Give the extent of all Trypanosoma brucei.
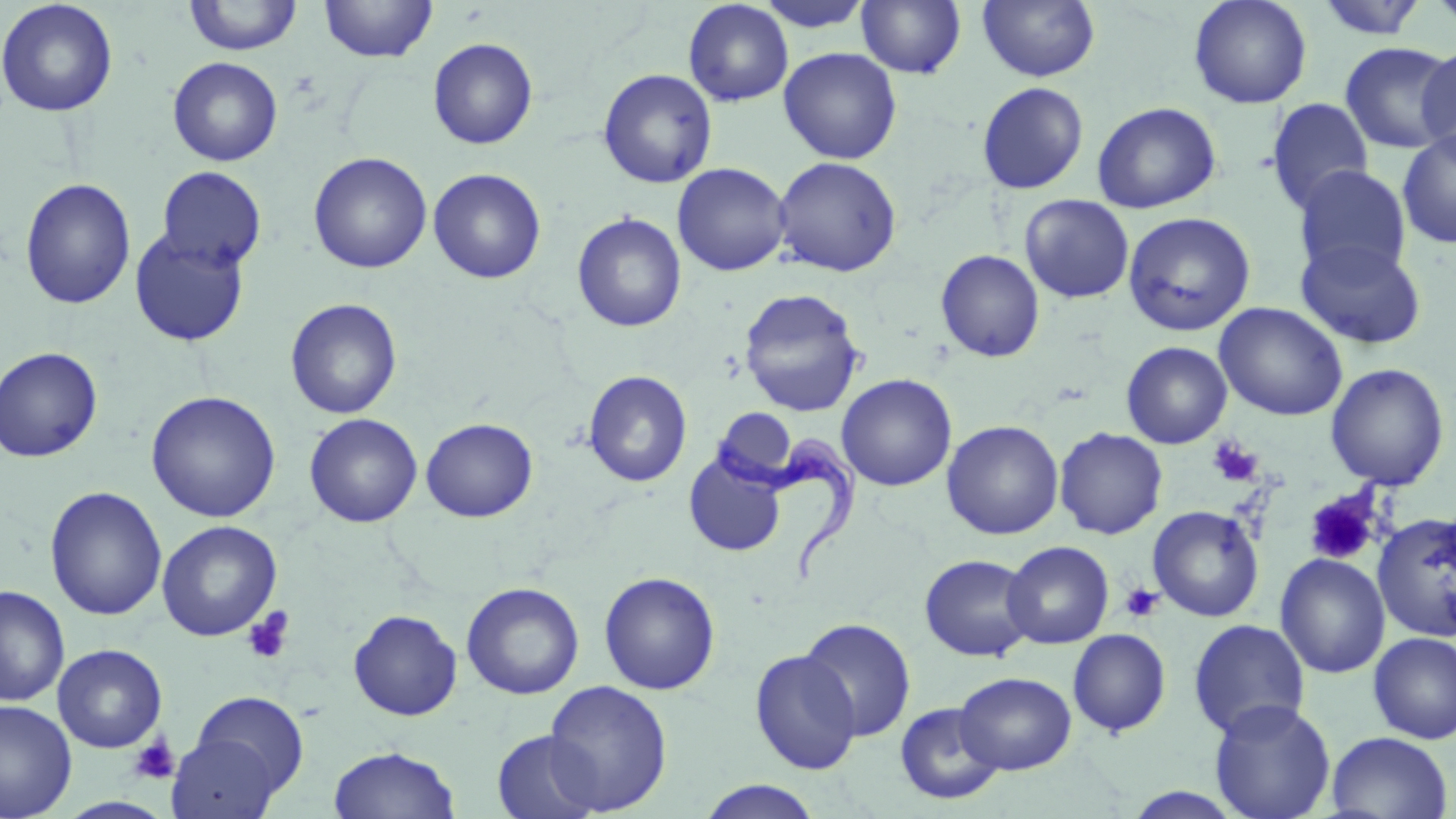

Approximate bounding boxes as named x1/y1/x2/y2 corners in pixels.
Trypanosoma brucei: (x1=710, y1=433, x2=865, y2=581).

Summary:
  - Uninfected red blood cell locations: (x1=183, y1=0, x2=304, y2=56), (x1=319, y1=0, x2=438, y2=63), (x1=754, y1=0, x2=874, y2=33), (x1=978, y1=0, x2=1100, y2=82), (x1=1188, y1=0, x2=1312, y2=109), (x1=1314, y1=0, x2=1429, y2=41), (x1=1427, y1=0, x2=1456, y2=32), (x1=0, y1=1, x2=119, y2=117), (x1=683, y1=1, x2=794, y2=107), (x1=856, y1=1, x2=966, y2=78), (x1=427, y1=37, x2=538, y2=149), (x1=1339, y1=41, x2=1456, y2=154), (x1=1418, y1=45, x2=1456, y2=162), (x1=778, y1=47, x2=902, y2=164), (x1=167, y1=56, x2=283, y2=166), (x1=597, y1=68, x2=718, y2=188), (x1=977, y1=82, x2=1088, y2=195), (x1=1265, y1=98, x2=1374, y2=216), (x1=1092, y1=101, x2=1221, y2=213), (x1=1397, y1=129, x2=1456, y2=250), (x1=308, y1=152, x2=433, y2=274), (x1=772, y1=156, x2=902, y2=277), (x1=672, y1=162, x2=791, y2=276), (x1=1293, y1=165, x2=1411, y2=281), (x1=156, y1=166, x2=267, y2=272), (x1=428, y1=168, x2=546, y2=284), (x1=20, y1=178, x2=136, y2=310), (x1=1019, y1=194, x2=1134, y2=303), (x1=1122, y1=211, x2=1256, y2=336), (x1=571, y1=212, x2=687, y2=333), (x1=129, y1=227, x2=250, y2=347), (x1=1295, y1=239, x2=1426, y2=349), (x1=935, y1=250, x2=1045, y2=362), (x1=738, y1=289, x2=865, y2=417), (x1=285, y1=298, x2=402, y2=419), (x1=1214, y1=302, x2=1348, y2=421), (x1=1121, y1=341, x2=1232, y2=449), (x1=0, y1=347, x2=103, y2=462), (x1=1325, y1=363, x2=1449, y2=490), (x1=583, y1=370, x2=693, y2=487), (x1=836, y1=374, x2=957, y2=491), (x1=145, y1=390, x2=281, y2=522), (x1=713, y1=407, x2=801, y2=486), (x1=304, y1=413, x2=422, y2=527), (x1=420, y1=418, x2=538, y2=522), (x1=941, y1=420, x2=1064, y2=540), (x1=1054, y1=427, x2=1167, y2=540), (x1=684, y1=453, x2=787, y2=557), (x1=44, y1=487, x2=167, y2=620), (x1=1148, y1=505, x2=1265, y2=621), (x1=1373, y1=513, x2=1456, y2=641), (x1=156, y1=520, x2=282, y2=641), (x1=1002, y1=541, x2=1114, y2=649), (x1=1274, y1=553, x2=1391, y2=679), (x1=919, y1=554, x2=1036, y2=661), (x1=599, y1=571, x2=721, y2=695), (x1=461, y1=582, x2=584, y2=700), (x1=0, y1=585, x2=70, y2=706), (x1=348, y1=609, x2=463, y2=721), (x1=799, y1=617, x2=916, y2=741), (x1=1188, y1=619, x2=1310, y2=740), (x1=1067, y1=628, x2=1171, y2=737), (x1=1368, y1=631, x2=1456, y2=743), (x1=52, y1=643, x2=167, y2=752), (x1=750, y1=649, x2=862, y2=775), (x1=954, y1=671, x2=1077, y2=775), (x1=543, y1=680, x2=672, y2=815), (x1=187, y1=691, x2=309, y2=799), (x1=1209, y1=699, x2=1336, y2=819), (x1=0, y1=700, x2=77, y2=819), (x1=894, y1=702, x2=1005, y2=806), (x1=492, y1=730, x2=603, y2=819), (x1=1326, y1=731, x2=1453, y2=818), (x1=166, y1=732, x2=282, y2=818), (x1=328, y1=745, x2=461, y2=819), (x1=696, y1=780, x2=824, y2=818), (x1=1119, y1=786, x2=1250, y2=818)
  - Platelet locations: (x1=1207, y1=437, x2=1264, y2=488), (x1=1303, y1=489, x2=1382, y2=566), (x1=1120, y1=583, x2=1164, y2=623), (x1=242, y1=607, x2=295, y2=665), (x1=128, y1=735, x2=181, y2=785)
  - Slide-level diagnosis: Trypanosoma brucei
  - Modality: optical microscopy
  - Preparation: thin blood film
  - Magnification: 1000x
  - Field of view: single
  - Image size: 1456×819 pixels
  - Stain: May-Grünwald-Giemsa